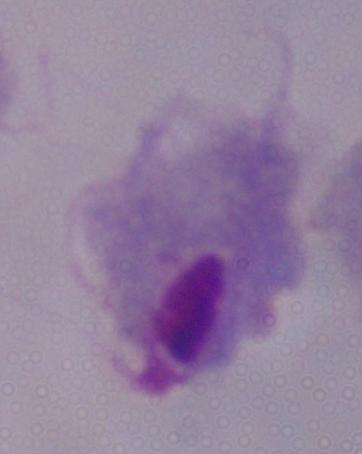

magnification = 1000x
identification = trichomonad
modality = micrograph